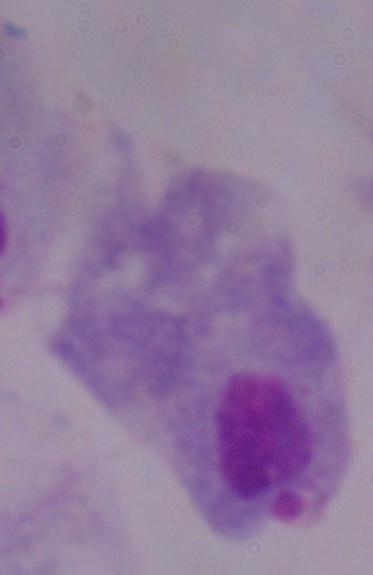 Micrograph. A trichomonad is shown. 1000x magnification.